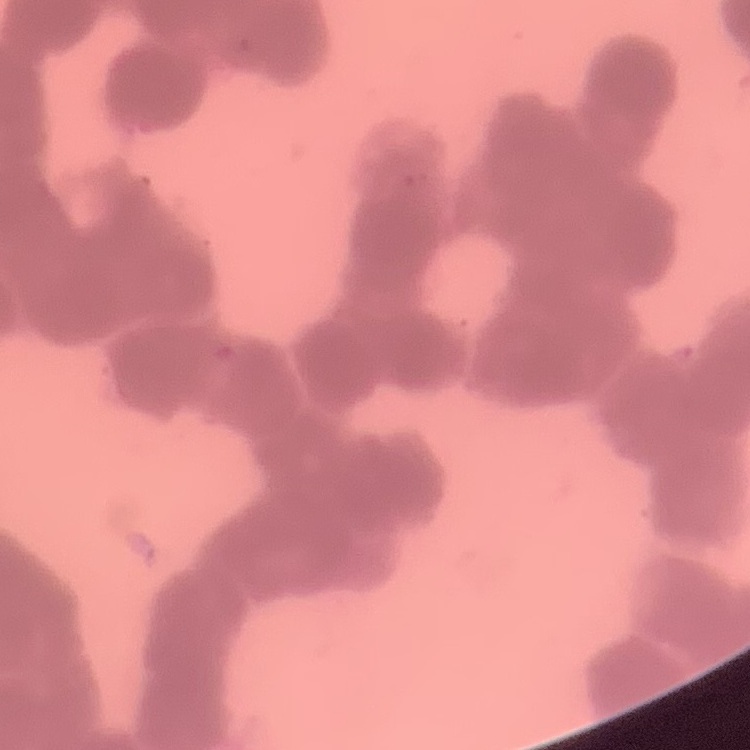
erythrocyte_morphology: rouleaux formation
preparation: thin blood smear
stain: Field's or Giemsa
image_type: square crop of a larger photomicrograph